Classify this cell by malaria status.
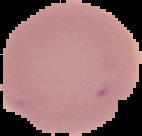
It is uninfected.

Segmented cell region on a black background. From a thin blood film. Image is 142×136 pixels.